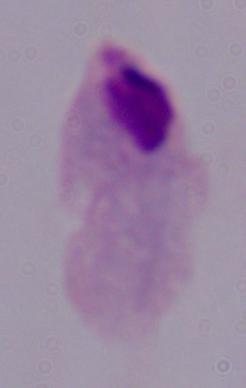
Micrograph. A trichomonad is seen. Captured at 1000x magnification.